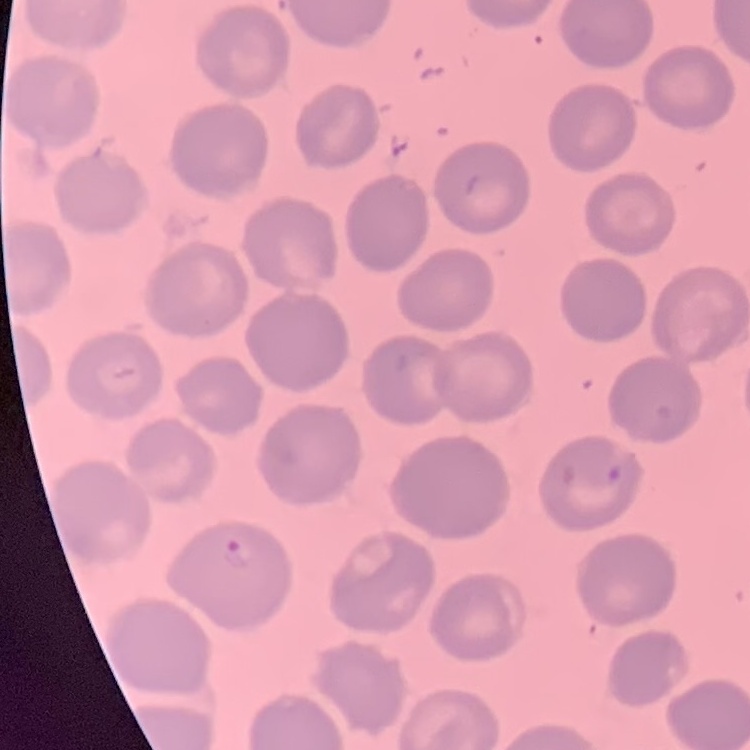
The red blood cells show no rouleaux formation. Square crop of a larger photomicrograph. Thin blood smear. Field's or Giemsa stain.